Report the malaria status of this cell.
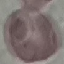
It is uninfected.

Summary:
  - Capture: smartphone camera at the microscope eyepiece
  - Preparation: thin blood smear
  - Stain: Giemsa
  - Image type: automatically extracted cell patch, resized to 64 × 64 pixels